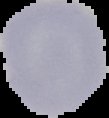

{
  "preparation": "thin blood film",
  "image_type": "segmented cell region on a black background",
  "malaria_status": "uninfected",
  "image_size": "109×118 pixels"
}